Name the blood parasite species.
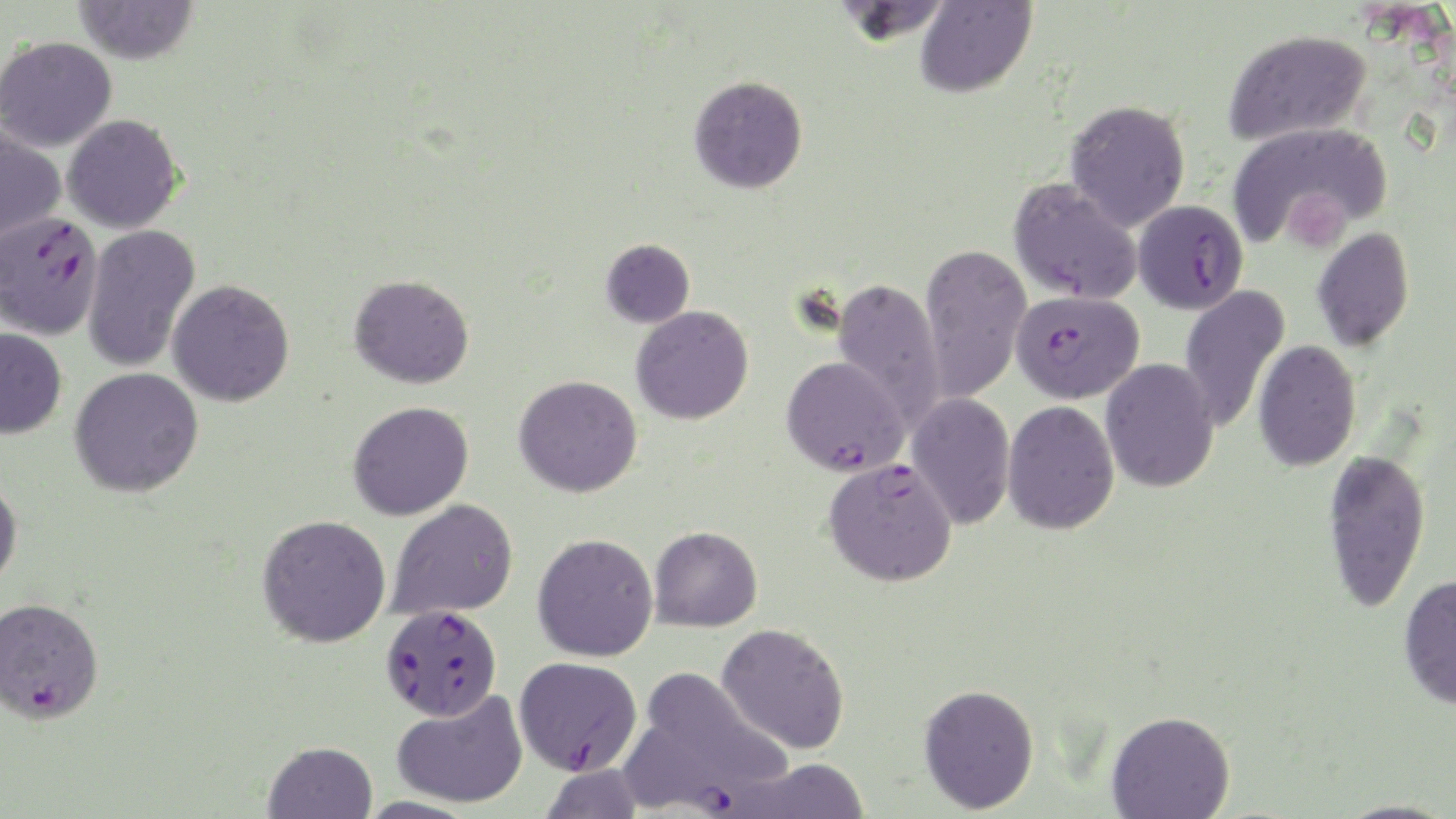

Plasmodium falciparum.

Approximate bounding boxes as [x1, y1, x2, y2] in pixels. Uninfected red blood cell locations: [73, 0, 199, 65], [915, 0, 1036, 97], [1222, 28, 1372, 145], [0, 35, 117, 152], [689, 75, 808, 194], [1065, 99, 1191, 231], [62, 114, 183, 233], [1227, 119, 1391, 250], [0, 124, 66, 245], [1008, 178, 1142, 305], [83, 224, 200, 373], [1312, 226, 1414, 352], [601, 238, 695, 328], [919, 243, 1032, 405], [349, 274, 474, 388], [830, 278, 946, 429], [167, 279, 295, 407], [1179, 285, 1291, 433], [631, 305, 754, 425], [0, 328, 67, 439], [1253, 340, 1361, 472], [1101, 358, 1219, 493], [70, 367, 204, 497], [513, 375, 642, 497], [906, 392, 1015, 529], [348, 400, 474, 520], [1002, 401, 1120, 535], [1321, 447, 1431, 613], [0, 474, 23, 590], [387, 498, 518, 620], [257, 514, 391, 647], [649, 526, 762, 632], [532, 532, 659, 661], [1398, 573, 1456, 710], [717, 622, 851, 754], [643, 669, 789, 784], [918, 683, 1040, 814], [391, 689, 528, 809], [1106, 710, 1235, 819], [263, 741, 378, 819], [729, 758, 871, 818], [537, 762, 645, 819], [1332, 799, 1454, 819]. Plasmodium falciparum-infected red blood cell locations: [1134, 199, 1248, 314], [0, 211, 103, 340], [1011, 288, 1144, 404], [781, 356, 908, 476], [822, 457, 958, 587], [0, 596, 104, 724], [381, 603, 503, 722], [514, 656, 642, 775], [622, 725, 744, 817]. Single field of view. Optical microscopy. May-Grünwald-Giemsa stain. 1000x magnification. Thin blood film. Image is 1456×819 pixels.